Name the parasite shown.
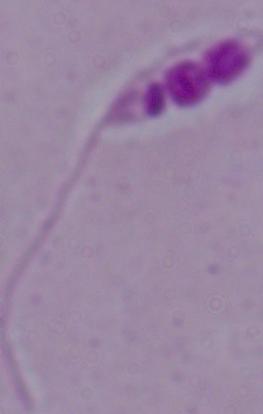
This is Leishmania.

Captured at 1000x magnification. Micrograph.